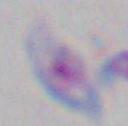
identification = Toxoplasma gondii
magnification = 1000x
modality = micrograph